Locate every white blood cell.
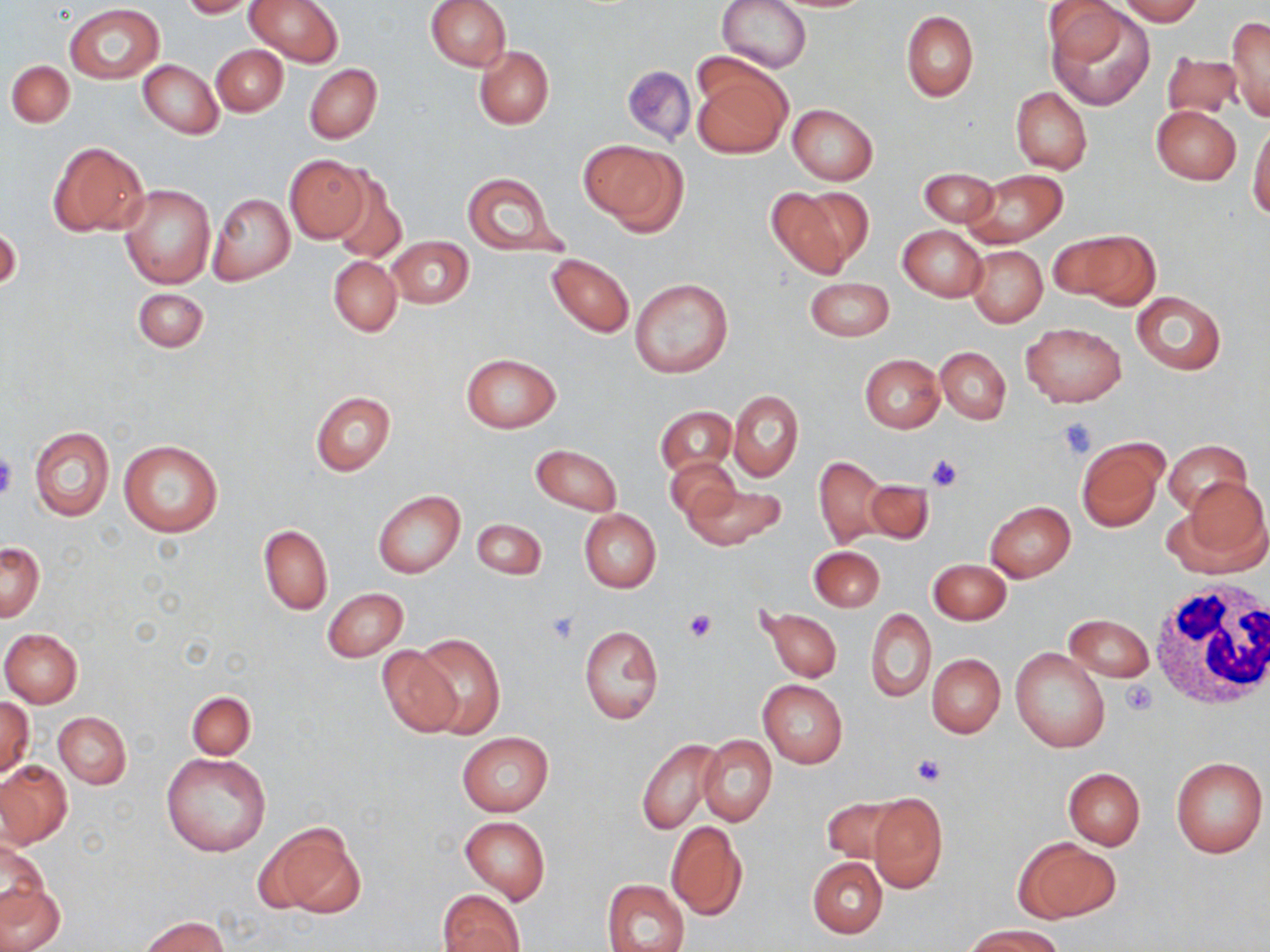

Approximate bounding boxes as [x1, y1, x2, y2] in pixels.
White blood cells: [1148, 580, 1267, 709].

Platelet locations: [1054, 418, 1098, 459], [0, 450, 18, 501], [925, 452, 965, 490], [684, 609, 717, 642], [545, 612, 580, 644], [1122, 679, 1157, 715], [911, 755, 946, 788]. Uninfected red blood cell locations: [177, 0, 260, 18], [246, 0, 345, 67], [425, 0, 511, 70], [719, 0, 810, 73], [1044, 0, 1129, 70], [1118, 0, 1202, 24], [65, 5, 164, 84], [1050, 7, 1154, 109], [902, 11, 979, 101], [1226, 15, 1270, 121], [211, 45, 288, 116], [475, 46, 553, 128], [1162, 48, 1240, 123], [691, 58, 790, 158], [6, 60, 74, 128], [139, 60, 222, 138], [305, 63, 382, 144], [622, 64, 696, 146], [1011, 87, 1091, 175], [787, 104, 877, 185], [1150, 105, 1240, 185], [1249, 119, 1270, 223], [578, 140, 685, 232], [47, 141, 150, 236], [285, 154, 369, 242], [918, 168, 999, 226], [328, 169, 407, 264], [964, 169, 1067, 247], [462, 173, 562, 255], [118, 184, 216, 287], [767, 185, 870, 277], [208, 193, 295, 285], [1, 225, 21, 296], [897, 226, 986, 300], [1058, 229, 1157, 309], [388, 236, 473, 309], [967, 246, 1047, 326], [547, 253, 634, 338], [329, 256, 401, 335], [630, 277, 732, 378], [805, 278, 894, 341], [132, 287, 209, 352], [1130, 291, 1225, 375], [1021, 322, 1127, 406], [936, 346, 1011, 423], [462, 352, 560, 433], [859, 354, 944, 433], [729, 389, 803, 482], [309, 391, 395, 476], [656, 407, 736, 478], [30, 426, 113, 521], [1074, 436, 1167, 533], [1165, 438, 1252, 513], [117, 439, 223, 537], [531, 445, 620, 516], [813, 455, 888, 548], [664, 456, 738, 521], [862, 478, 935, 545], [1170, 478, 1270, 578], [679, 482, 787, 550], [373, 490, 465, 578], [985, 501, 1076, 581], [579, 509, 661, 593], [471, 518, 546, 580], [258, 526, 332, 614], [1, 542, 44, 621], [809, 546, 884, 611], [928, 558, 1011, 625], [322, 588, 409, 662], [758, 604, 842, 683], [866, 608, 935, 701], [1064, 614, 1153, 683], [579, 625, 663, 725], [1, 628, 83, 708], [411, 635, 504, 738], [377, 646, 462, 738], [1011, 648, 1109, 753], [926, 654, 1005, 738], [757, 679, 848, 768], [187, 691, 255, 759], [1, 697, 34, 777], [53, 712, 131, 788], [457, 731, 552, 815], [697, 735, 777, 827], [637, 739, 726, 835], [162, 752, 272, 858], [1170, 755, 1268, 858], [0, 761, 72, 848], [1063, 767, 1145, 851], [868, 792, 947, 893], [818, 795, 906, 865], [460, 815, 550, 904], [258, 818, 366, 921], [664, 820, 748, 920], [1013, 836, 1121, 922], [1, 838, 49, 917], [808, 857, 887, 938], [603, 879, 689, 952], [0, 880, 65, 952], [438, 889, 525, 952], [143, 915, 229, 952], [963, 923, 1065, 952]. Slide-level diagnosis: negative for blood parasites. May-Grünwald-Giemsa stain. One field of a larger specimen. 1000x magnification. Thin blood film. Light microscopy. Image is 1270×952 pixels.